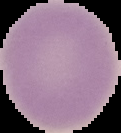 Image is 121×133 pixels. From a thin blood film. Cell region segmented out of the field of view; the surrounding area is masked to black. Malaria status: uninfected.